Outline each blood parasite and name the species.
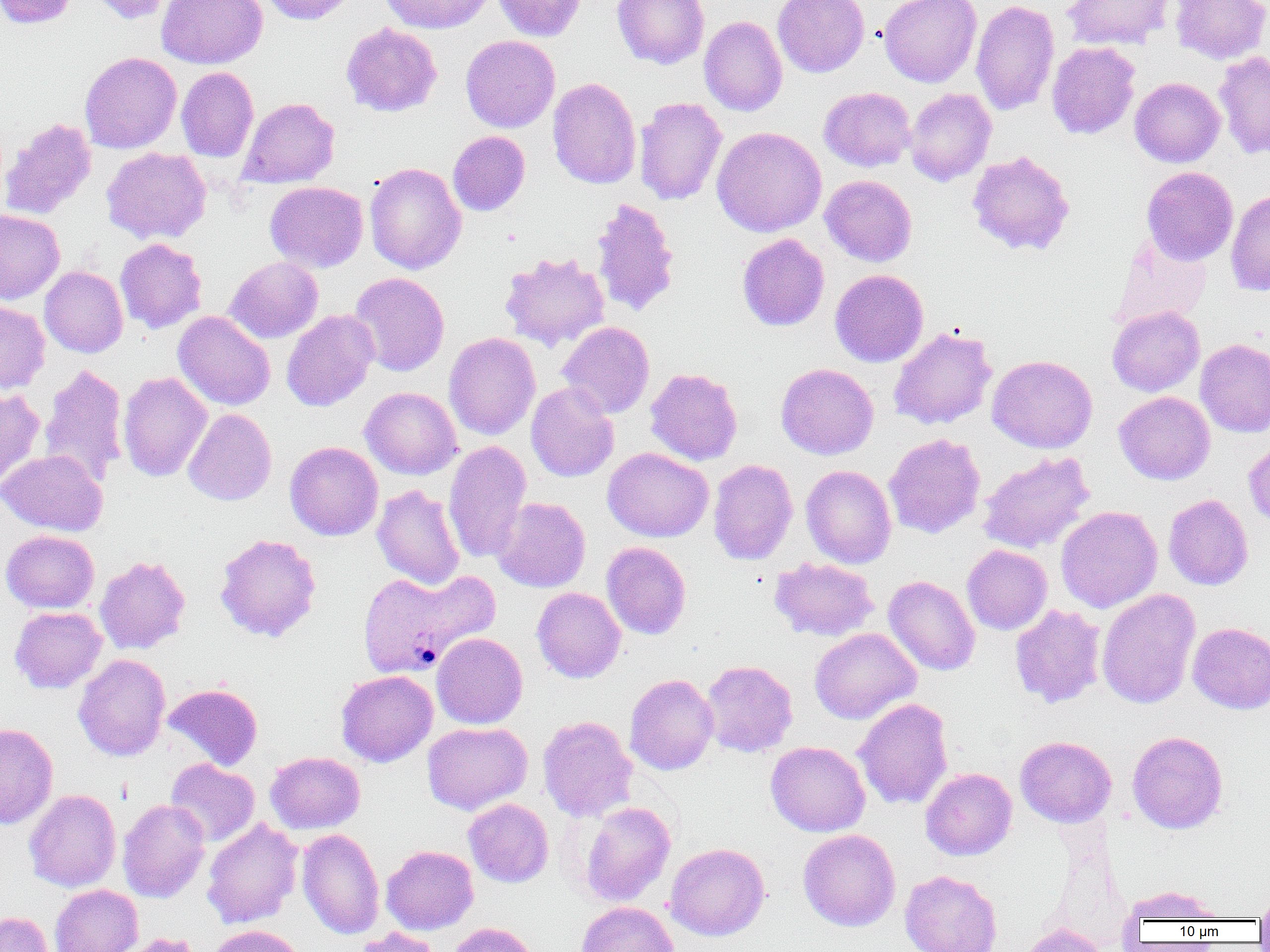
Approximate bounding boxes as (x1,y1)-(x2,y2) corner pairs in pixels.
Plasmodium vivax-infected red blood cells: (357,567)-(499,679).
No Plasmodium falciparum, Plasmodium ovale, Plasmodium malariae, Babesia divergens, or Trypanosoma brucei observed.

Uninfected red blood cell locations: (0,0)-(77,29), (85,0)-(176,25), (156,0)-(267,69), (259,0)-(360,25), (378,0)-(497,33), (492,0)-(587,41), (612,0)-(709,69), (773,0)-(870,77), (879,0)-(981,87), (971,0)-(1060,116), (1061,0)-(1174,50), (1170,0)-(1270,64), (699,16)-(787,116), (340,23)-(443,117), (460,35)-(560,132), (1046,41)-(1141,140), (1213,50)-(1270,160), (79,52)-(181,153), (176,66)-(259,162), (547,77)-(641,189), (1130,77)-(1225,167), (819,87)-(916,172), (904,88)-(996,186), (238,97)-(340,188), (634,97)-(727,206), (1,118)-(96,219), (711,127)-(827,236), (448,131)-(530,215), (101,147)-(211,244), (966,151)-(1076,257), (364,162)-(466,275), (1141,166)-(1238,265), (820,175)-(917,267), (265,181)-(368,272), (1226,188)-(1270,296), (590,197)-(680,318), (0,209)-(65,304), (737,233)-(829,332), (1111,233)-(1212,330), (115,238)-(207,334), (499,252)-(610,352), (224,257)-(323,343), (39,266)-(128,358), (830,269)-(929,367), (349,272)-(450,376), (0,300)-(50,394), (1107,306)-(1204,396), (188,309)-(368,408), (281,309)-(379,411), (173,310)-(275,410), (557,321)-(655,418), (889,326)-(997,430), (443,332)-(540,440), (1195,338)-(1270,438), (987,354)-(1098,453), (38,363)-(128,489), (776,363)-(878,460), (645,367)-(743,466), (118,371)-(212,482), (526,382)-(619,482), (360,387)-(461,479), (0,388)-(45,494), (1114,391)-(1215,485), (183,408)-(277,506), (883,433)-(985,538), (1244,438)-(1270,528), (285,441)-(383,540), (443,441)-(532,563), (602,448)-(713,542), (0,449)-(107,535), (977,451)-(1095,553), (708,459)-(798,565), (801,465)-(897,568), (372,484)-(465,590), (1163,494)-(1253,590), (492,497)-(591,592), (1056,506)-(1162,613), (1,530)-(100,613), (214,533)-(322,642), (601,541)-(692,640), (962,544)-(1053,635), (95,555)-(191,654), (769,557)-(879,641), (883,575)-(981,676), (532,587)-(626,683), (1097,588)-(1201,709), (1009,604)-(1106,709), (10,606)-(107,693), (1187,622)-(1270,714), (810,628)-(921,724), (432,633)-(528,728), (73,654)-(170,761), (700,660)-(798,757), (336,670)-(438,767), (624,673)-(719,775), (163,683)-(263,770), (853,698)-(953,809), (538,715)-(638,822), (422,721)-(532,815), (0,723)-(58,829), (1127,730)-(1228,834), (1014,736)-(1117,827), (766,741)-(870,837), (265,751)-(365,834), (165,758)-(260,846), (920,767)-(1017,861), (24,789)-(121,892), (463,798)-(553,887), (118,799)-(210,902), (579,801)-(676,906), (202,818)-(303,929), (297,827)-(384,940), (798,829)-(901,931), (665,843)-(769,941), (381,845)-(478,934), (899,870)-(1002,952), (50,884)-(143,952), (1121,885)-(1224,924), (1254,887)-(1270,925), (576,901)-(678,952), (0,911)-(53,952), (447,922)-(539,952), (1021,923)-(1109,952), (207,924)-(308,952), (353,927)-(443,952), (113,933)-(204,952). Slide-level diagnosis: Plasmodium vivax. One field of a larger specimen. Thin blood smear. 1000x magnification. Optical microscopy. Image is 1270×952 pixels.